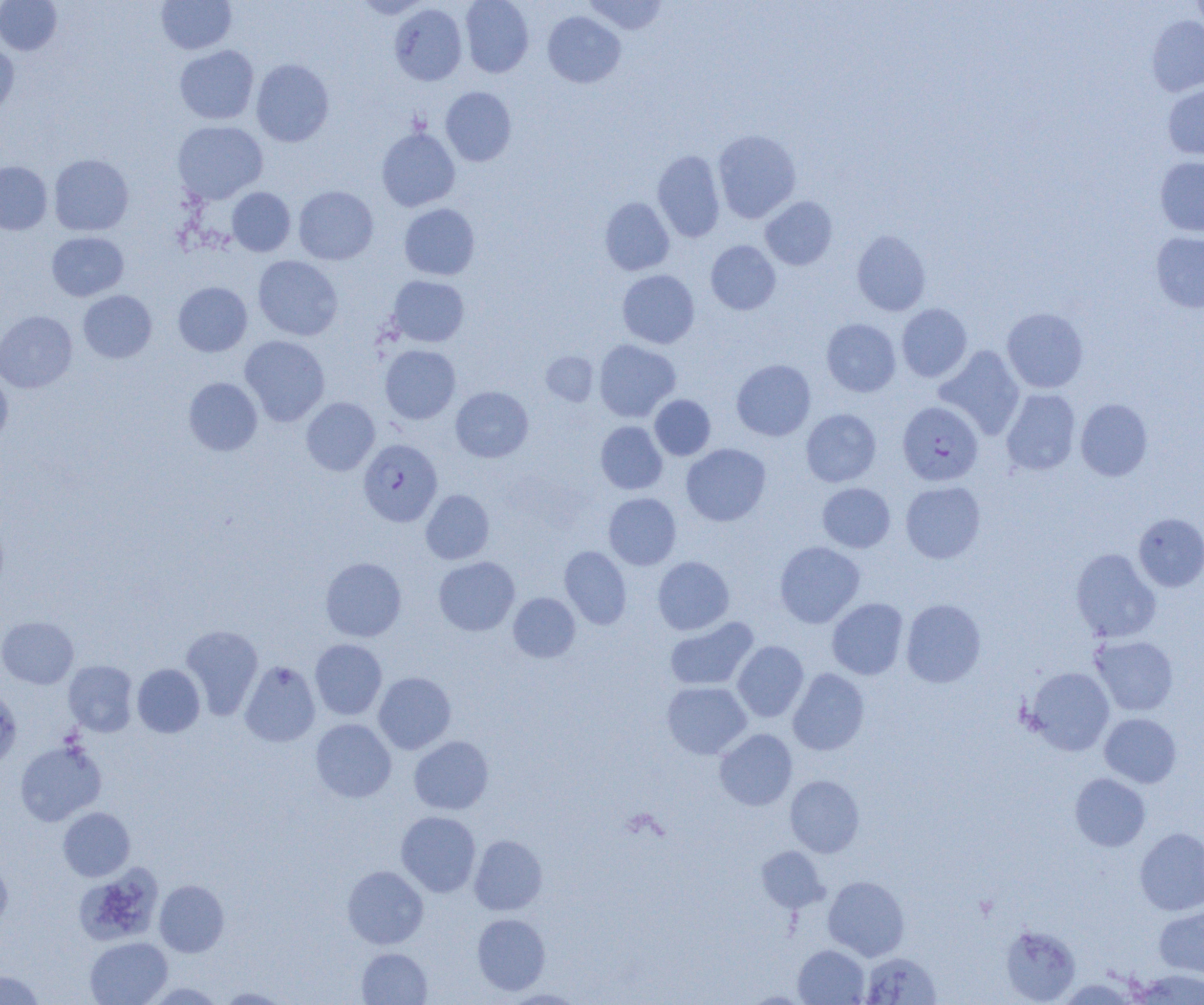
slide-level diagnosis = Plasmodium falciparum
image size = 1204×1005 pixels
preparation = thin blood film
uninfected red blood cell locations = approximate bounding boxes as named x1/y1/x2/y2 corners in pixels: (x1=156, y1=0, x2=237, y2=54), (x1=353, y1=0, x2=432, y2=19), (x1=460, y1=0, x2=534, y2=77), (x1=583, y1=0, x2=668, y2=35), (x1=1189, y1=0, x2=1204, y2=37), (x1=0, y1=1, x2=62, y2=55), (x1=389, y1=3, x2=467, y2=85), (x1=542, y1=11, x2=626, y2=88), (x1=1146, y1=15, x2=1204, y2=97), (x1=0, y1=41, x2=19, y2=114), (x1=175, y1=45, x2=259, y2=124), (x1=251, y1=59, x2=334, y2=146), (x1=1162, y1=84, x2=1204, y2=160), (x1=440, y1=87, x2=516, y2=166), (x1=172, y1=121, x2=267, y2=204), (x1=376, y1=127, x2=460, y2=211), (x1=712, y1=129, x2=801, y2=223), (x1=652, y1=150, x2=725, y2=242), (x1=49, y1=154, x2=133, y2=236), (x1=1155, y1=156, x2=1204, y2=237), (x1=0, y1=161, x2=52, y2=235), (x1=293, y1=185, x2=378, y2=265), (x1=227, y1=187, x2=295, y2=256), (x1=760, y1=196, x2=838, y2=270), (x1=600, y1=197, x2=674, y2=275), (x1=399, y1=203, x2=480, y2=280), (x1=852, y1=230, x2=931, y2=316), (x1=47, y1=231, x2=129, y2=301), (x1=1151, y1=231, x2=1204, y2=312), (x1=706, y1=240, x2=781, y2=314), (x1=253, y1=255, x2=343, y2=340), (x1=617, y1=270, x2=699, y2=348), (x1=386, y1=275, x2=469, y2=347), (x1=173, y1=282, x2=252, y2=356), (x1=78, y1=290, x2=156, y2=363), (x1=897, y1=304, x2=972, y2=382), (x1=1002, y1=307, x2=1088, y2=393), (x1=0, y1=311, x2=77, y2=393), (x1=822, y1=318, x2=901, y2=397), (x1=239, y1=335, x2=330, y2=426), (x1=594, y1=339, x2=680, y2=422), (x1=380, y1=345, x2=461, y2=424), (x1=934, y1=345, x2=1025, y2=440), (x1=541, y1=351, x2=599, y2=405), (x1=731, y1=359, x2=815, y2=440), (x1=0, y1=370, x2=13, y2=449), (x1=183, y1=377, x2=262, y2=456), (x1=451, y1=386, x2=533, y2=462), (x1=1001, y1=388, x2=1080, y2=476), (x1=650, y1=394, x2=716, y2=460), (x1=301, y1=397, x2=380, y2=475), (x1=1075, y1=398, x2=1153, y2=481), (x1=801, y1=408, x2=881, y2=487), (x1=595, y1=421, x2=667, y2=494), (x1=681, y1=443, x2=771, y2=526), (x1=900, y1=481, x2=985, y2=563), (x1=817, y1=483, x2=895, y2=552), (x1=421, y1=489, x2=494, y2=564), (x1=603, y1=493, x2=681, y2=570), (x1=1133, y1=513, x2=1204, y2=592), (x1=775, y1=541, x2=865, y2=628), (x1=559, y1=545, x2=632, y2=629), (x1=1071, y1=548, x2=1161, y2=642), (x1=433, y1=556, x2=520, y2=636), (x1=653, y1=556, x2=734, y2=635), (x1=320, y1=557, x2=407, y2=642), (x1=508, y1=592, x2=581, y2=662), (x1=827, y1=598, x2=908, y2=679), (x1=901, y1=599, x2=986, y2=687), (x1=0, y1=616, x2=79, y2=688), (x1=665, y1=617, x2=759, y2=691), (x1=180, y1=624, x2=263, y2=719), (x1=1090, y1=635, x2=1179, y2=716), (x1=310, y1=639, x2=387, y2=720), (x1=732, y1=640, x2=809, y2=722), (x1=63, y1=660, x2=138, y2=737), (x1=240, y1=660, x2=321, y2=747), (x1=132, y1=664, x2=205, y2=737), (x1=1025, y1=666, x2=1115, y2=755), (x1=788, y1=668, x2=869, y2=755), (x1=373, y1=672, x2=456, y2=754), (x1=662, y1=681, x2=751, y2=759), (x1=0, y1=688, x2=22, y2=768), (x1=1100, y1=713, x2=1181, y2=788), (x1=310, y1=719, x2=396, y2=802), (x1=715, y1=729, x2=797, y2=810), (x1=409, y1=736, x2=494, y2=814), (x1=15, y1=739, x2=107, y2=825), (x1=1070, y1=773, x2=1151, y2=851), (x1=785, y1=775, x2=864, y2=857), (x1=58, y1=807, x2=135, y2=881), (x1=396, y1=811, x2=481, y2=897), (x1=1135, y1=828, x2=1204, y2=915), (x1=469, y1=834, x2=548, y2=915), (x1=756, y1=846, x2=828, y2=913), (x1=0, y1=857, x2=12, y2=931), (x1=342, y1=865, x2=428, y2=949), (x1=75, y1=866, x2=162, y2=947), (x1=823, y1=876, x2=909, y2=961), (x1=154, y1=880, x2=229, y2=957), (x1=1154, y1=906, x2=1204, y2=977), (x1=472, y1=913, x2=550, y2=995), (x1=1000, y1=924, x2=1080, y2=1003), (x1=85, y1=937, x2=172, y2=1005), (x1=794, y1=944, x2=869, y2=1004), (x1=357, y1=948, x2=432, y2=1004), (x1=861, y1=952, x2=941, y2=1004), (x1=1130, y1=969, x2=1204, y2=1004), (x1=0, y1=970, x2=45, y2=1004), (x1=1055, y1=978, x2=1141, y2=1004), (x1=215, y1=987, x2=292, y2=1004), (x1=501, y1=989, x2=586, y2=1004), (x1=741, y1=991, x2=813, y2=1004)
modality = optical microscopy
Plasmodium falciparum-infected red blood cell locations = approximate bounding boxes as named x1/y1/x2/y2 corners in pixels: (x1=898, y1=401, x2=983, y2=485), (x1=358, y1=439, x2=442, y2=526)
field of view = one of a larger specimen
magnification = 1000x